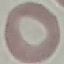

Malaria status: uninfected. Photographed with a smartphone camera at the microscope eyepiece. Giemsa stain. Thin blood film. Cell patch, automatically extracted from a larger field of view and resized to 64 × 64 pixels.